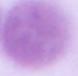

Captured at 1000x magnification. A red blood cell is seen. Micrograph.